Outline each blood parasite and name the species.
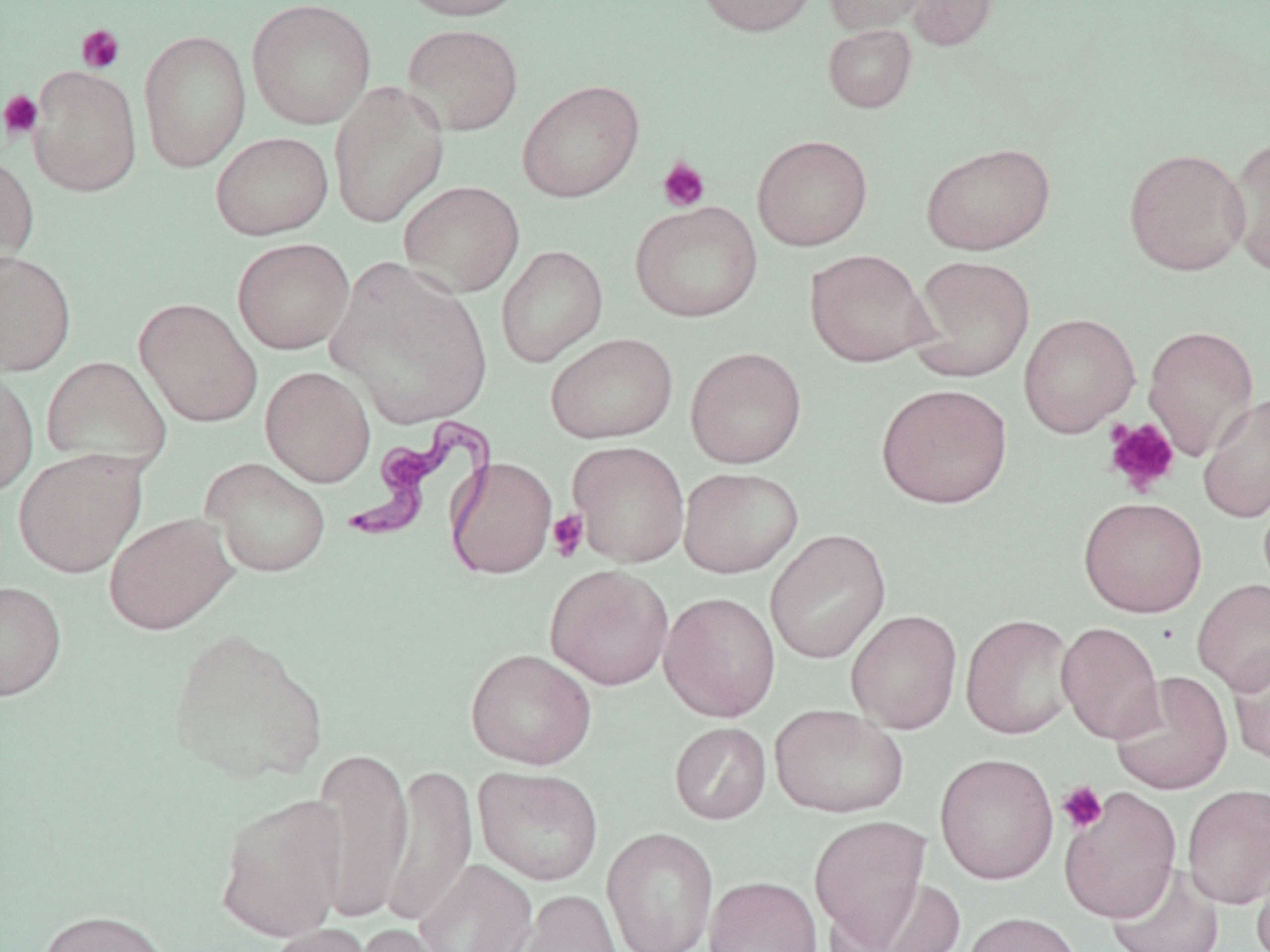
Approximate bounding boxes as named x1/y1/x2/y2 corners in pixels.
Trypanosoma brucei: (x1=342, y1=413, x2=498, y2=564).
No Plasmodium falciparum, Plasmodium ovale, Plasmodium malariae, Plasmodium vivax, or Babesia divergens observed.

{
  "slide_level_diagnosis": "Trypanosoma brucei",
  "image_size": "1270×952 pixels",
  "magnification": "1000x",
  "platelet_locations": "approximate bounding boxes as named x1/y1/x2/y2 corners in pixels: (x1=76, y1=24, x2=126, y2=74), (x1=0, y1=89, x2=44, y2=141), (x1=657, y1=157, x2=710, y2=212), (x1=1103, y1=418, x2=1180, y2=496), (x1=547, y1=509, x2=589, y2=562), (x1=1057, y1=781, x2=1109, y2=834)",
  "preparation": "thin blood film",
  "modality": "light microscopy",
  "uninfected_red_blood_cell_locations": "approximate bounding boxes as named x1/y1/x2/y2 corners in pixels: (x1=246, y1=0, x2=377, y2=130), (x1=395, y1=0, x2=531, y2=21), (x1=693, y1=0, x2=820, y2=37), (x1=824, y1=0, x2=932, y2=35), (x1=904, y1=0, x2=999, y2=51), (x1=401, y1=22, x2=524, y2=136), (x1=823, y1=24, x2=917, y2=113), (x1=138, y1=29, x2=252, y2=172), (x1=28, y1=65, x2=142, y2=197), (x1=517, y1=79, x2=644, y2=203), (x1=328, y1=81, x2=450, y2=228), (x1=210, y1=131, x2=334, y2=240), (x1=752, y1=134, x2=873, y2=251), (x1=1225, y1=137, x2=1270, y2=274), (x1=921, y1=142, x2=1056, y2=255), (x1=1123, y1=147, x2=1251, y2=276), (x1=0, y1=151, x2=40, y2=276), (x1=398, y1=180, x2=525, y2=298), (x1=630, y1=201, x2=763, y2=322), (x1=232, y1=237, x2=354, y2=354), (x1=496, y1=244, x2=608, y2=367), (x1=805, y1=248, x2=934, y2=367), (x1=0, y1=249, x2=77, y2=377), (x1=909, y1=255, x2=1035, y2=381), (x1=327, y1=258, x2=494, y2=429), (x1=134, y1=297, x2=263, y2=428), (x1=1018, y1=313, x2=1140, y2=437), (x1=1143, y1=325, x2=1259, y2=459), (x1=545, y1=332, x2=678, y2=444), (x1=685, y1=347, x2=807, y2=468), (x1=41, y1=355, x2=171, y2=475), (x1=261, y1=366, x2=375, y2=487), (x1=0, y1=367, x2=39, y2=498), (x1=876, y1=383, x2=1013, y2=509), (x1=1197, y1=392, x2=1270, y2=523), (x1=568, y1=441, x2=690, y2=567), (x1=13, y1=449, x2=147, y2=577), (x1=446, y1=456, x2=558, y2=579), (x1=201, y1=458, x2=331, y2=578), (x1=678, y1=466, x2=804, y2=578), (x1=1078, y1=496, x2=1207, y2=618), (x1=103, y1=512, x2=238, y2=635), (x1=766, y1=529, x2=891, y2=664), (x1=544, y1=564, x2=674, y2=690), (x1=1192, y1=578, x2=1270, y2=694), (x1=0, y1=580, x2=67, y2=701), (x1=659, y1=592, x2=781, y2=722), (x1=846, y1=609, x2=963, y2=733), (x1=960, y1=614, x2=1078, y2=739), (x1=1056, y1=621, x2=1165, y2=744), (x1=166, y1=626, x2=329, y2=785), (x1=1227, y1=645, x2=1270, y2=766), (x1=465, y1=648, x2=597, y2=769), (x1=1109, y1=671, x2=1233, y2=796), (x1=769, y1=704, x2=909, y2=818), (x1=670, y1=722, x2=771, y2=825), (x1=310, y1=746, x2=413, y2=923), (x1=935, y1=752, x2=1059, y2=885), (x1=383, y1=763, x2=478, y2=928), (x1=472, y1=766, x2=604, y2=886), (x1=1182, y1=783, x2=1270, y2=908), (x1=1058, y1=787, x2=1182, y2=923), (x1=214, y1=792, x2=347, y2=942), (x1=809, y1=815, x2=931, y2=947), (x1=601, y1=827, x2=719, y2=952), (x1=1251, y1=849, x2=1270, y2=952), (x1=414, y1=859, x2=538, y2=952), (x1=1106, y1=863, x2=1226, y2=952), (x1=704, y1=875, x2=823, y2=952), (x1=846, y1=877, x2=968, y2=952), (x1=512, y1=889, x2=622, y2=952), (x1=35, y1=908, x2=174, y2=952), (x1=961, y1=911, x2=1084, y2=952), (x1=263, y1=922, x2=378, y2=952), (x1=350, y1=923, x2=451, y2=952)",
  "field_of_view": "single",
  "stain": "May-Grünwald-Giemsa"
}